Locate platelets.
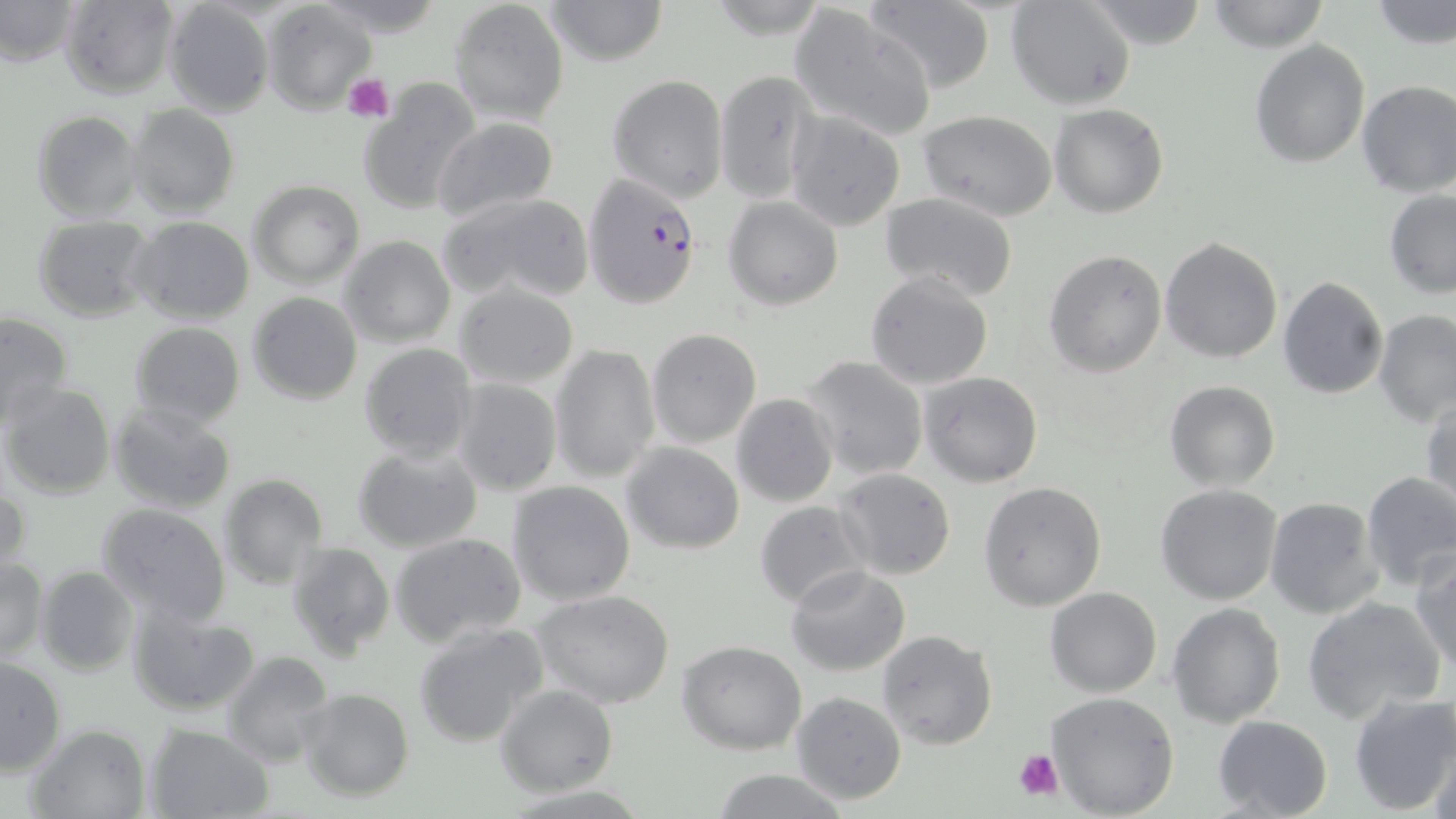

Approximate bounding boxes as (x1, y1, x2, y2) in pixels.
Platelets: (343, 73, 395, 123), (1013, 746, 1064, 802).

Summary:
  - Plasmodium falciparum-infected red blood cell locations: (584, 172, 700, 308)
  - Uninfected red blood cell locations: (311, 0, 448, 37), (448, 0, 570, 124), (543, 0, 670, 66), (1007, 0, 1136, 110), (1081, 0, 1209, 49), (1205, 0, 1331, 52), (1370, 0, 1456, 51), (0, 1, 78, 67), (60, 1, 180, 98), (161, 1, 275, 118), (864, 1, 995, 93), (263, 2, 375, 116), (788, 3, 940, 142), (1249, 38, 1370, 169), (712, 71, 822, 201), (606, 74, 728, 203), (357, 75, 481, 214), (1354, 78, 1456, 197), (1050, 103, 1171, 218), (127, 104, 240, 219), (32, 110, 143, 223), (785, 110, 907, 230), (918, 111, 1060, 221), (432, 116, 559, 218), (248, 180, 364, 288), (1384, 188, 1456, 298), (435, 192, 596, 304), (880, 192, 1019, 302), (724, 196, 844, 310), (32, 215, 155, 320), (128, 217, 255, 325), (340, 235, 455, 348), (1159, 237, 1283, 364), (1044, 247, 1166, 377), (866, 271, 994, 389), (1277, 275, 1389, 400), (455, 282, 580, 389), (247, 292, 362, 405), (1374, 309, 1455, 428), (0, 311, 74, 428), (130, 321, 246, 429), (646, 328, 761, 446), (359, 343, 477, 463), (550, 344, 660, 483), (800, 356, 929, 481), (917, 371, 1044, 488), (451, 378, 562, 496), (1164, 381, 1282, 492), (2, 383, 116, 500), (731, 393, 838, 507), (1422, 397, 1456, 517), (107, 401, 236, 515), (621, 442, 745, 553), (354, 443, 483, 554), (835, 469, 955, 579), (1359, 470, 1456, 590), (219, 474, 328, 590), (506, 480, 635, 604), (978, 481, 1108, 612), (1, 483, 30, 577), (1155, 484, 1284, 605), (1263, 497, 1382, 619), (754, 500, 872, 608), (95, 503, 232, 625), (389, 532, 527, 649), (286, 542, 394, 661), (1411, 549, 1456, 676), (0, 558, 50, 662), (787, 565, 910, 675), (36, 566, 138, 676), (1044, 586, 1162, 697), (533, 589, 675, 708), (1302, 595, 1446, 726), (1167, 602, 1287, 728), (128, 604, 262, 716), (413, 622, 552, 750), (876, 630, 998, 750), (677, 641, 806, 754), (220, 651, 335, 768), (0, 656, 67, 777), (496, 685, 618, 797), (299, 688, 415, 802), (1044, 691, 1180, 818), (1348, 691, 1456, 815), (790, 692, 906, 806), (1211, 715, 1333, 819), (26, 723, 152, 819), (144, 725, 272, 818), (1428, 737, 1456, 819), (711, 769, 851, 819)
  - Slide-level diagnosis: Plasmodium falciparum
  - Stain: May-Grünwald-Giemsa
  - Image size: 1456×819 pixels
  - Magnification: 1000x
  - Field of view: single
  - Preparation: thin blood smear
  - Modality: light microscopy